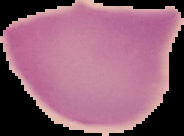
image size = 184×136 pixels
result = negative for malaria parasites
image type = segmented cell region on a black background
preparation = thin blood smear